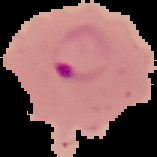
Summary:
  - Preparation: thin blood smear
  - Malaria status: parasitized
  - Image type: cell region segmented out of the field of view; surrounding area masked to black
  - Image size: 157×157 pixels